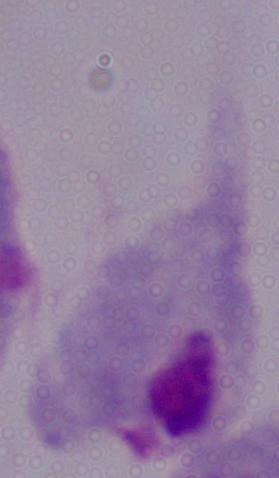

1000x magnification. A trichomonad is shown. Micrograph.